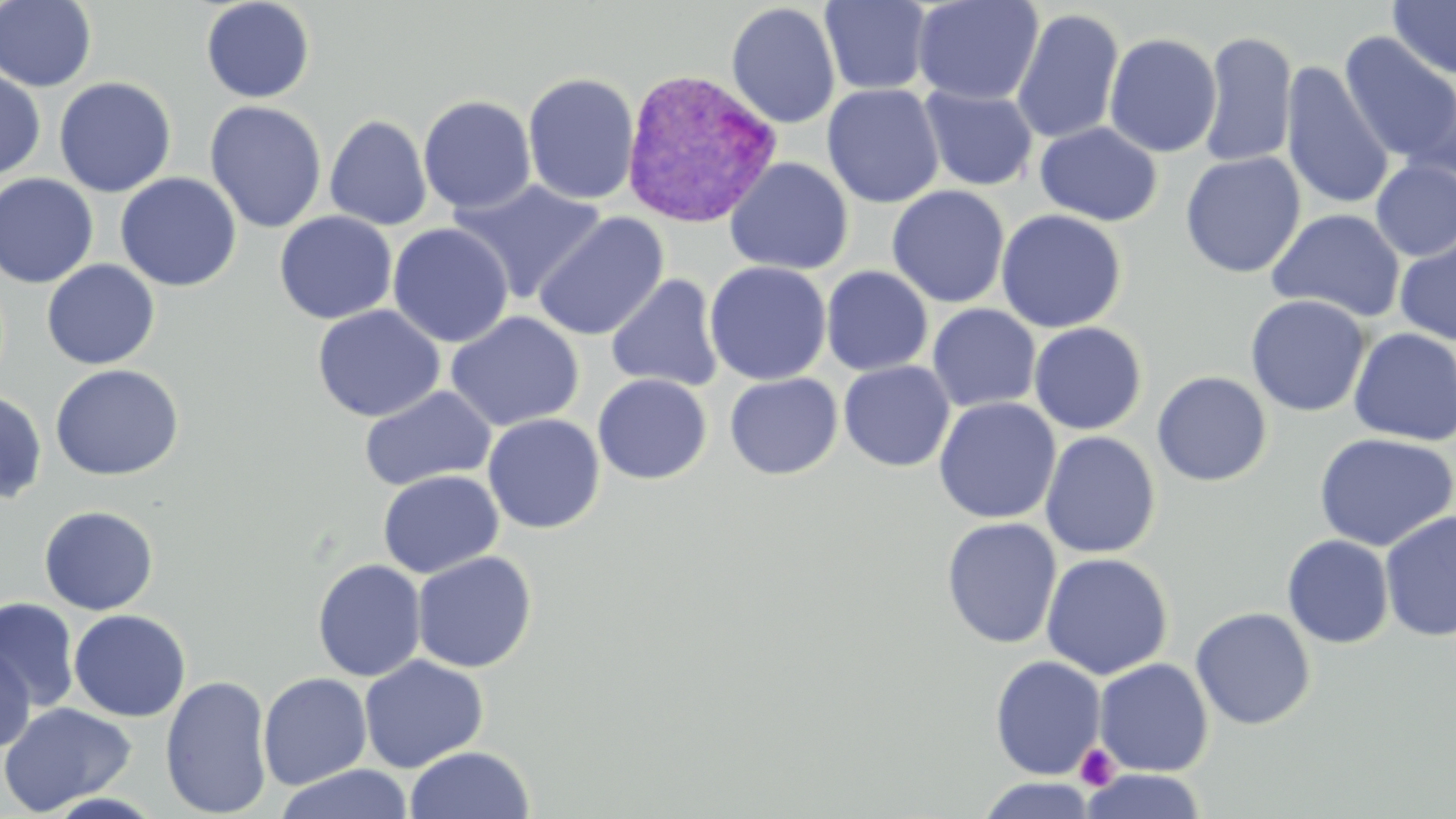

Approximate bounding boxes as named x1/y1/x2/y2 corners in pixels. Plasmodium vivax-infected red blood cell locations: (x1=620, y1=67, x2=781, y2=229). Platelet locations: (x1=1074, y1=743, x2=1120, y2=790). Uninfected red blood cell locations: (x1=0, y1=0, x2=98, y2=92), (x1=200, y1=0, x2=316, y2=104), (x1=911, y1=0, x2=1045, y2=106), (x1=1388, y1=0, x2=1456, y2=81), (x1=819, y1=1, x2=934, y2=96), (x1=726, y1=2, x2=841, y2=129), (x1=1011, y1=8, x2=1124, y2=146), (x1=1198, y1=29, x2=1298, y2=169), (x1=1104, y1=32, x2=1222, y2=158), (x1=1338, y1=32, x2=1456, y2=169), (x1=1281, y1=61, x2=1396, y2=211), (x1=0, y1=67, x2=46, y2=182), (x1=522, y1=72, x2=641, y2=205), (x1=1402, y1=74, x2=1456, y2=184), (x1=53, y1=77, x2=176, y2=198), (x1=822, y1=84, x2=945, y2=208), (x1=919, y1=85, x2=1038, y2=191), (x1=418, y1=95, x2=537, y2=214), (x1=204, y1=100, x2=328, y2=233), (x1=325, y1=114, x2=432, y2=231), (x1=1035, y1=121, x2=1163, y2=226), (x1=1180, y1=152, x2=1306, y2=278), (x1=725, y1=157, x2=854, y2=275), (x1=1371, y1=159, x2=1456, y2=262), (x1=115, y1=172, x2=242, y2=292), (x1=0, y1=173, x2=100, y2=289), (x1=449, y1=178, x2=606, y2=303), (x1=887, y1=185, x2=1010, y2=308), (x1=995, y1=208, x2=1127, y2=333), (x1=1267, y1=208, x2=1406, y2=323), (x1=274, y1=210, x2=398, y2=324), (x1=532, y1=212, x2=670, y2=341), (x1=387, y1=223, x2=514, y2=347), (x1=1394, y1=230, x2=1456, y2=346), (x1=41, y1=260, x2=160, y2=370), (x1=704, y1=261, x2=832, y2=386), (x1=821, y1=266, x2=933, y2=376), (x1=605, y1=274, x2=724, y2=393), (x1=1245, y1=294, x2=1370, y2=417), (x1=927, y1=303, x2=1042, y2=413), (x1=311, y1=304, x2=446, y2=422), (x1=445, y1=311, x2=584, y2=431), (x1=1028, y1=322, x2=1147, y2=435), (x1=1348, y1=328, x2=1456, y2=447), (x1=837, y1=361, x2=955, y2=472), (x1=49, y1=363, x2=184, y2=481), (x1=1152, y1=371, x2=1272, y2=487), (x1=724, y1=372, x2=842, y2=480), (x1=593, y1=373, x2=712, y2=484), (x1=359, y1=385, x2=496, y2=491), (x1=0, y1=389, x2=48, y2=506), (x1=932, y1=397, x2=1061, y2=524), (x1=483, y1=413, x2=605, y2=534), (x1=1039, y1=431, x2=1162, y2=559), (x1=1314, y1=432, x2=1455, y2=552), (x1=378, y1=470, x2=504, y2=578), (x1=39, y1=505, x2=159, y2=615), (x1=1379, y1=510, x2=1456, y2=643), (x1=941, y1=517, x2=1063, y2=649), (x1=1282, y1=534, x2=1394, y2=649), (x1=412, y1=551, x2=537, y2=673), (x1=1040, y1=552, x2=1174, y2=680), (x1=312, y1=559, x2=427, y2=682), (x1=0, y1=597, x2=80, y2=713), (x1=1190, y1=607, x2=1316, y2=730), (x1=68, y1=609, x2=191, y2=721), (x1=0, y1=643, x2=36, y2=754), (x1=359, y1=655, x2=488, y2=773), (x1=989, y1=655, x2=1106, y2=780), (x1=1093, y1=658, x2=1214, y2=777), (x1=258, y1=672, x2=372, y2=790), (x1=160, y1=674, x2=274, y2=818), (x1=0, y1=701, x2=138, y2=815), (x1=403, y1=745, x2=536, y2=819), (x1=273, y1=763, x2=414, y2=819), (x1=1080, y1=769, x2=1208, y2=818), (x1=974, y1=776, x2=1101, y2=819), (x1=39, y1=791, x2=168, y2=818). Slide-level diagnosis: Plasmodium vivax. Thin blood smear. Captured at 1000x magnification. One field of a larger specimen. Image is 1456×819 pixels. May-Grünwald-Giemsa-stained preparation. Light microscopy.